Outline platelets.
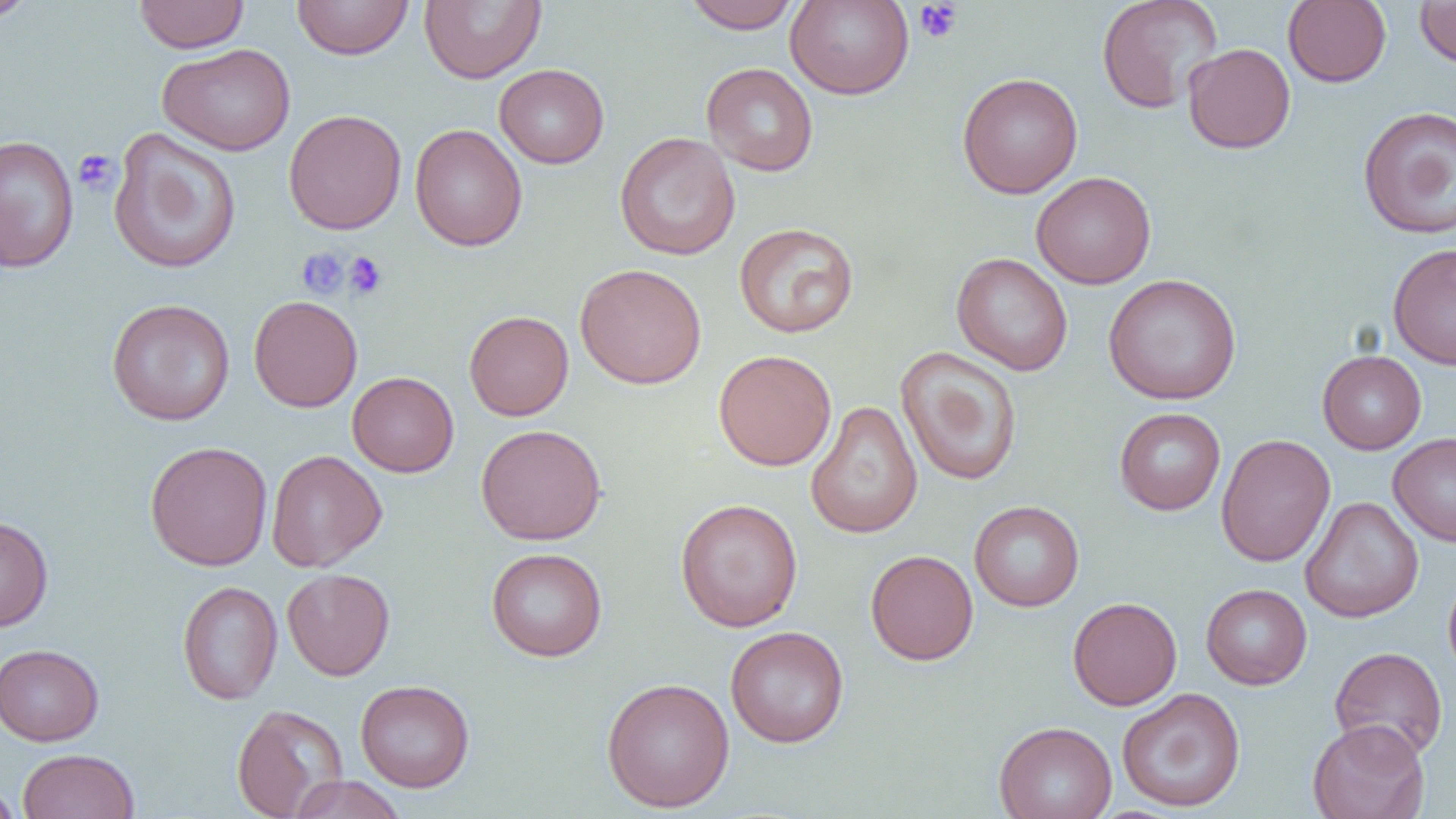

Approximate bounding boxes as (x1, y1, x2, y2) in pixels.
Platelets: (913, 1, 963, 44), (73, 149, 120, 197), (297, 247, 349, 299), (343, 251, 387, 300).

Uninfected red blood cell locations: (0, 0, 38, 24), (133, 0, 249, 53), (292, 0, 414, 59), (419, 0, 546, 83), (681, 0, 804, 33), (785, 0, 915, 99), (1096, 0, 1223, 113), (1282, 0, 1391, 88), (1415, 0, 1456, 68), (157, 43, 295, 156), (1183, 43, 1296, 154), (701, 62, 819, 177), (494, 64, 609, 168), (957, 72, 1083, 199), (1357, 105, 1456, 239), (283, 109, 407, 234), (410, 124, 528, 252), (108, 127, 242, 275), (614, 132, 740, 260), (0, 135, 79, 273), (1031, 171, 1156, 289), (733, 222, 859, 339), (1388, 242, 1456, 369), (951, 252, 1073, 376), (575, 262, 707, 389), (1103, 273, 1241, 405), (248, 295, 363, 412), (106, 298, 236, 425), (464, 310, 574, 421), (896, 347, 1023, 487), (713, 349, 836, 471), (1317, 350, 1427, 454), (347, 371, 459, 477), (805, 400, 923, 539), (1114, 408, 1226, 515), (476, 424, 607, 545), (1388, 432, 1456, 547), (1215, 434, 1335, 566), (144, 441, 273, 570), (266, 450, 387, 572), (1300, 496, 1424, 623), (675, 498, 803, 632), (969, 500, 1084, 611), (0, 515, 53, 632), (486, 547, 607, 661), (865, 550, 979, 665), (282, 568, 395, 680), (1443, 570, 1456, 683), (177, 580, 283, 705), (1201, 583, 1312, 690), (1067, 596, 1182, 710), (725, 625, 849, 748), (0, 644, 104, 746), (1329, 646, 1448, 761), (601, 677, 735, 812), (355, 679, 475, 792), (1117, 687, 1246, 812), (232, 703, 348, 818), (1307, 718, 1430, 819), (994, 721, 1117, 819), (18, 749, 140, 819), (287, 775, 408, 819), (0, 782, 22, 819). Slide-level diagnosis: no evidence of blood parasites. Image is 1456×819 pixels. Thin blood smear. 1000x magnification. Single field of view. Light microscopy.